Assess this cell for malaria.
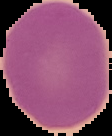

Uninfected.

Summary:
  - Image size: 112×136 pixels
  - Image type: segmented cell region with the area outside set to black
  - Preparation: thin blood smear